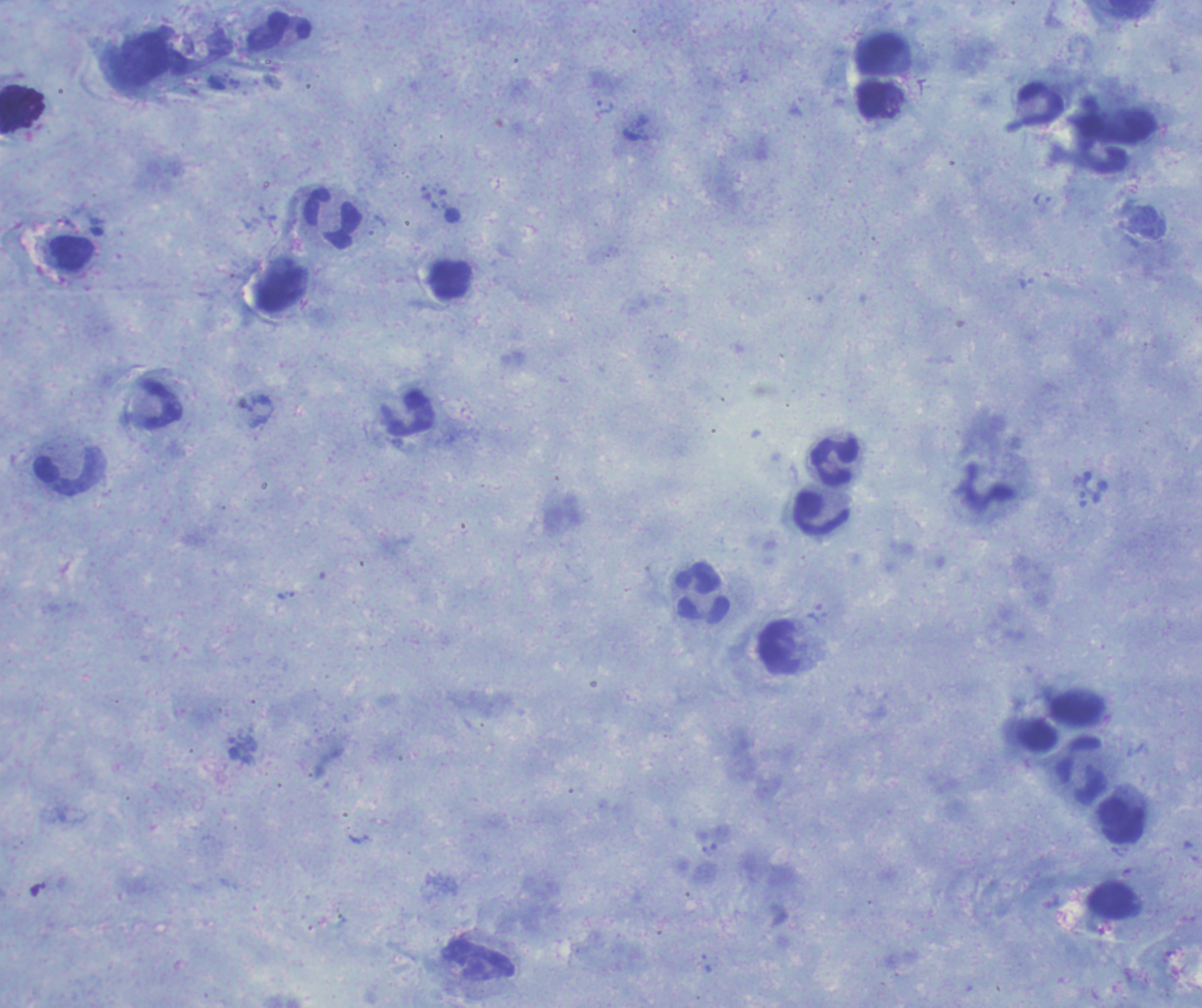

Approximate centers as {x, y} in pixels. Trophozoite locations: {606, 108}, {1042, 200}, {286, 595}, {817, 614}. Leukocyte locations: {280, 31}, {333, 218}, {450, 279}, {280, 290}, {157, 403}, {405, 412}, {835, 459}, {70, 471}, {821, 511}, {702, 593}, {780, 649}, {1083, 770}, {1120, 820}, {1110, 899}, {478, 961}. One field from this slide. Captured at 100x magnification. Result: positive for malaria parasites. Romanowsky stain. Coloration quality: good. Thick smear of blood. Previously used in an actual diagnosis. Background quality: satisfactory. Image is 1202×1008 pixels.